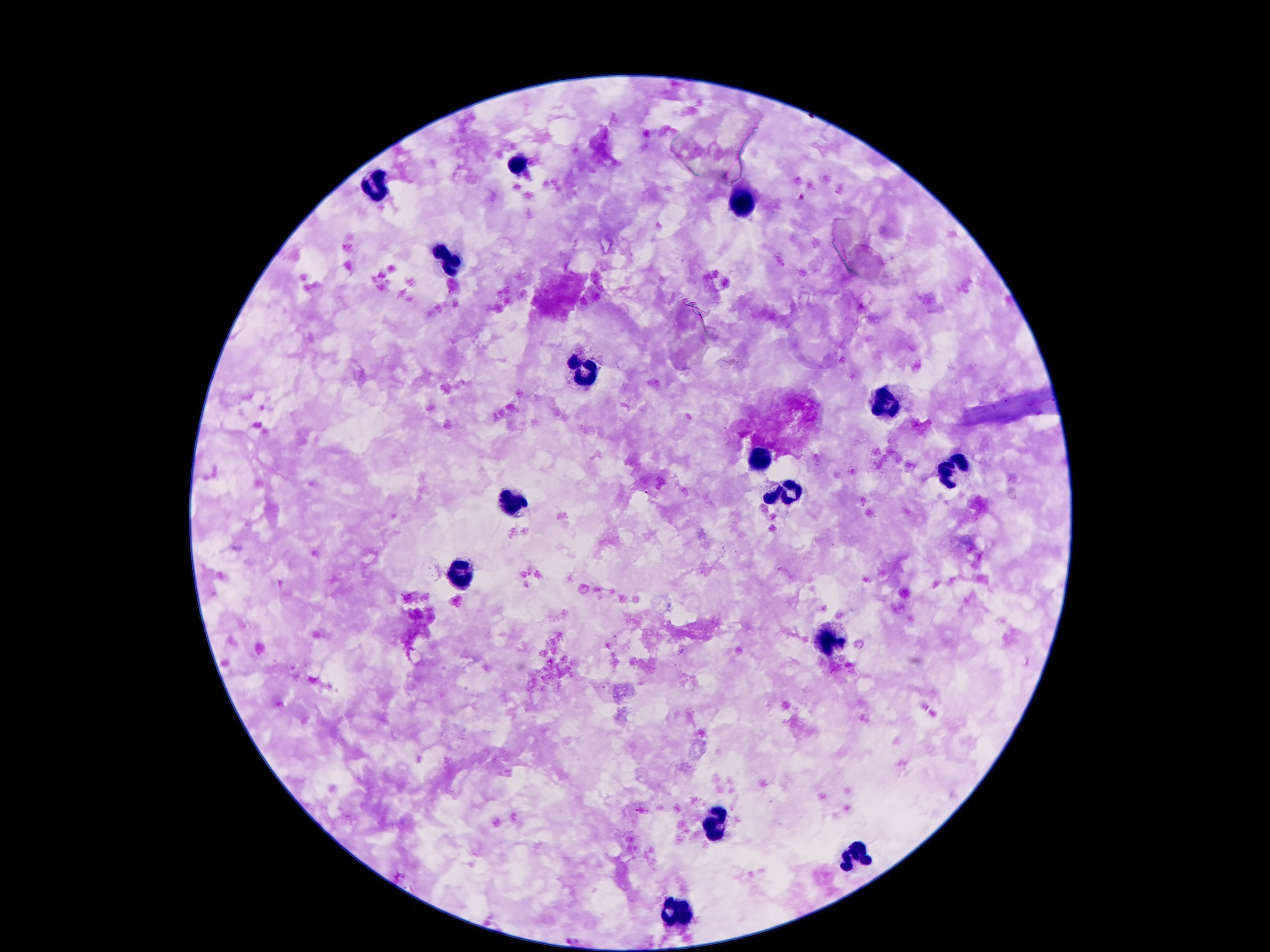 Approximate centers as (x, y) in pixels. Leukocyte locations: (516, 164), (378, 187), (741, 201), (448, 256), (583, 369), (884, 405), (757, 463), (952, 471), (792, 490), (509, 500), (458, 578), (831, 642), (712, 824), (854, 855), (677, 912). Patient malaria status: negative. Giemsa-stained preparation. One field from this slide. 100x magnification. Image is 1270×952 pixels. Thick peripheral-blood smear. Smartphone photograph taken through the microscope eyepiece.